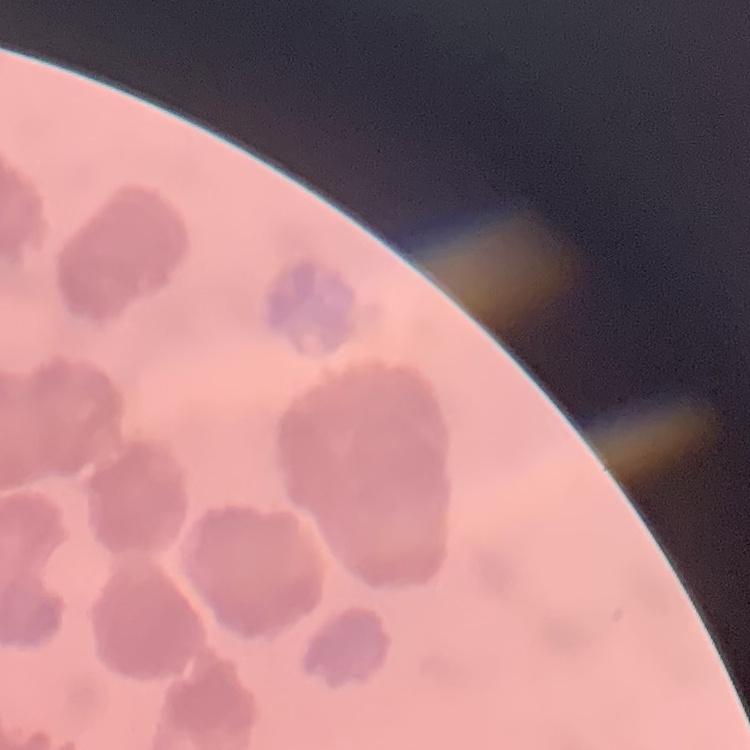
Summary:
  - Erythrocyte morphology: rouleaux formation
  - Image type: one tile cut from a larger photomicrograph
  - Preparation: thin peripheral smear
  - Stain: Field's or Giemsa